Report the malaria status of this cell.
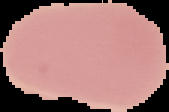
Uninfected.

image size = 169×112 pixels
preparation = thin blood film
image type = segmented cell region with the area outside set to black